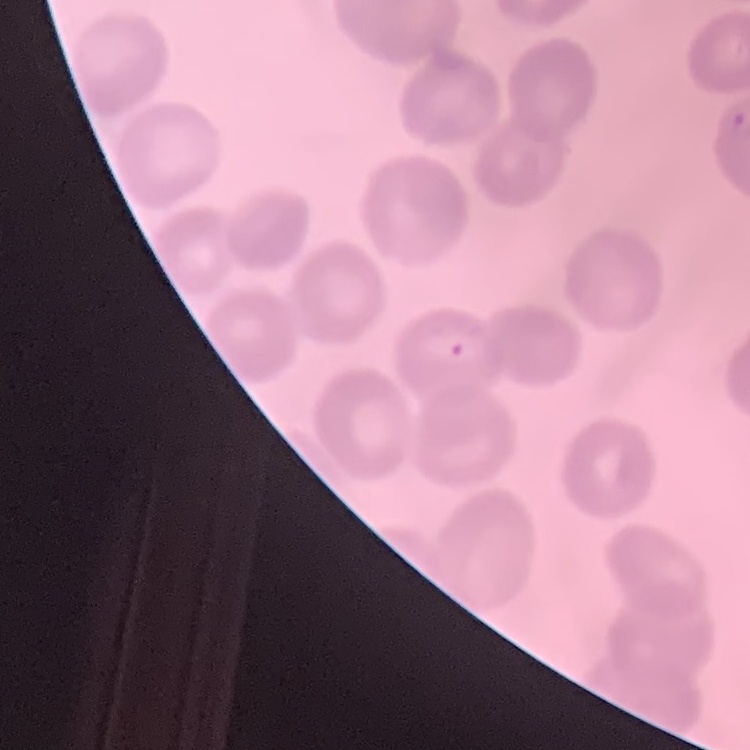

Summary:
  - Erythrocyte morphology: no rouleaux formation
  - Preparation: thin peripheral smear
  - Image type: square crop of a larger photomicrograph
  - Stain: Field's or Giemsa